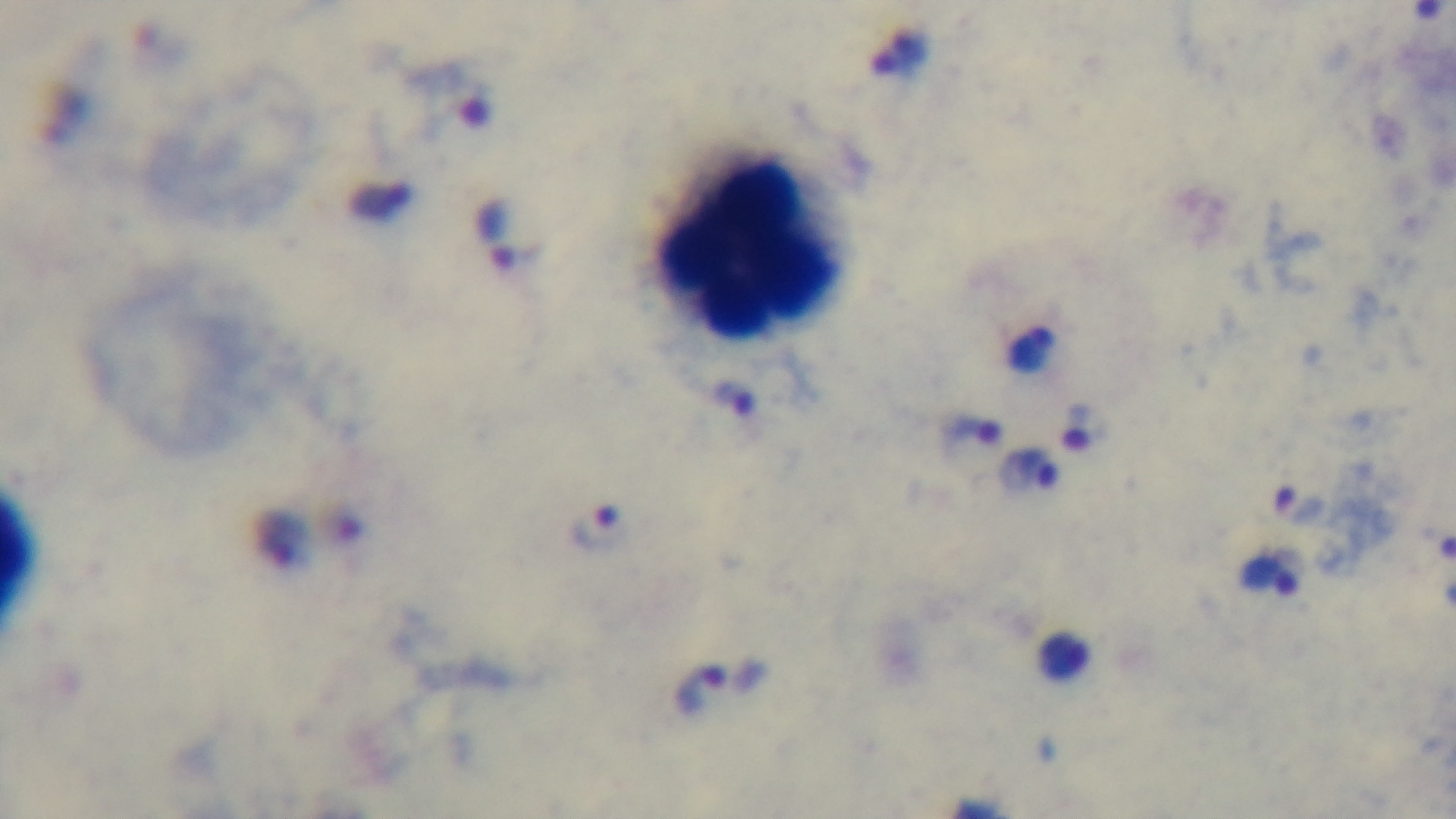
{
  "preparation": "thick smear",
  "malaria_status": "positive",
  "stain": "Giemsa",
  "objective": "100x oil immersion",
  "capture": "mounted 4K digital camera",
  "modality": "light microscopy",
  "field_of_view": "one from the slide"
}